Report the malaria status of this cell.
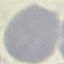

It is uninfected.

Acquired by smartphone through the microscope eyepiece. Cell patch, automatically extracted from a larger field of view and resized to 64 × 64 pixels. Thin smear of blood. Giemsa stain.